Assess the morphology of the erythrocytes.
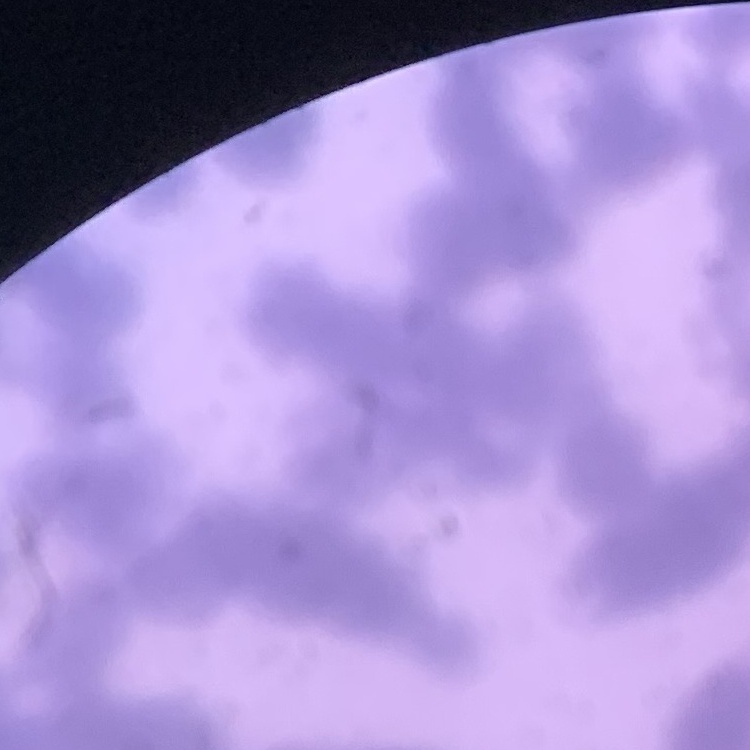

Rouleaux formation.

image_type: one tile cut from a larger photomicrograph
preparation: thin blood smear
stain: Field's or Giemsa